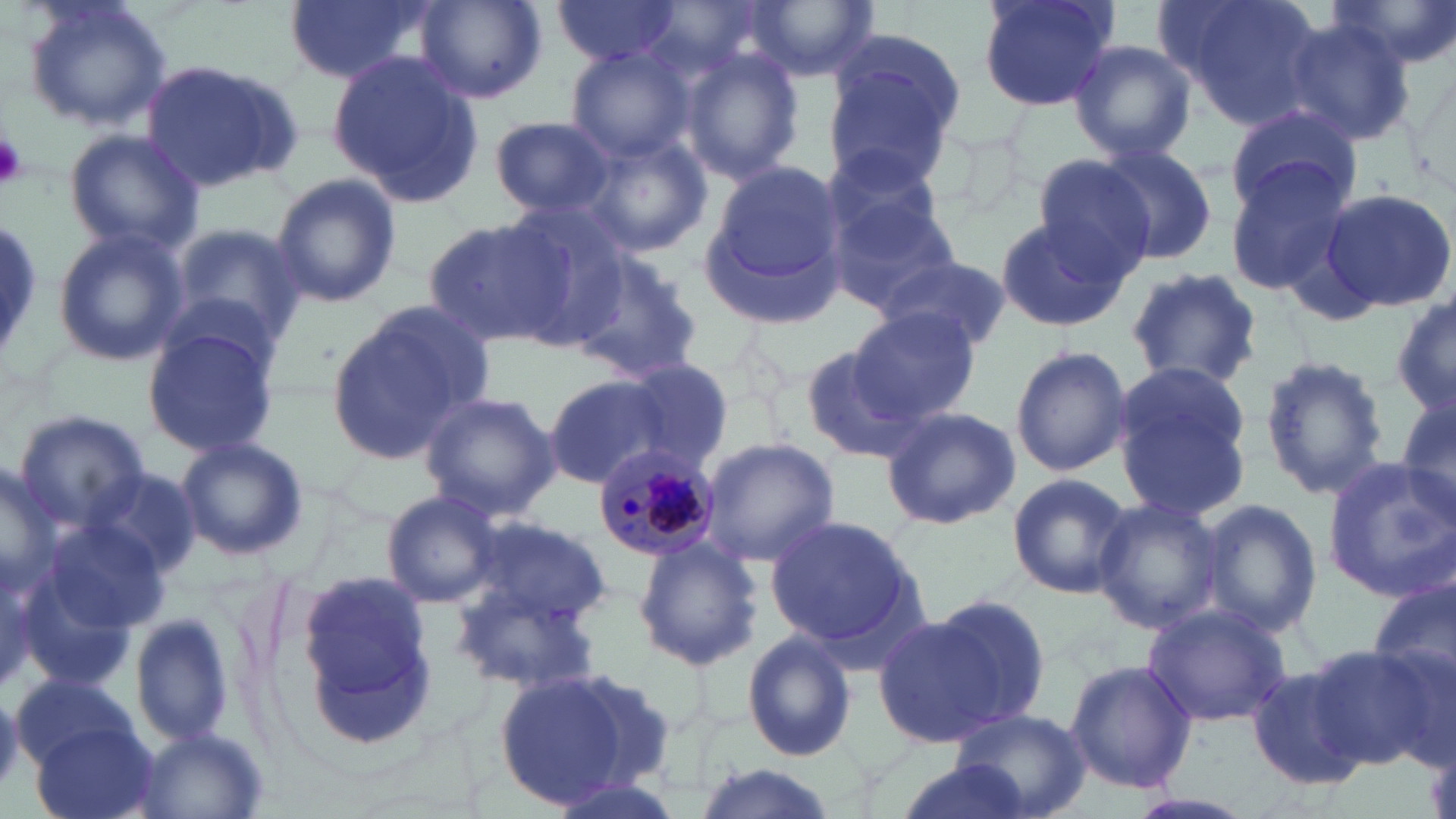
{
  "slide_level_diagnosis": "Plasmodium malariae",
  "uninfected_red_blood_cell_locations": "approximate bounding boxes as (x1, y1, x2, y2) in pixels: (23, 0, 170, 132), (282, 0, 432, 86), (415, 0, 549, 105), (551, 0, 685, 68), (975, 0, 1121, 112), (1159, 0, 1325, 127), (1334, 0, 1456, 70), (747, 1, 878, 82), (1277, 14, 1415, 150), (824, 33, 965, 176), (1067, 39, 1197, 163), (563, 45, 697, 164), (677, 46, 805, 184), (327, 51, 479, 205), (139, 58, 296, 196), (1223, 105, 1361, 213), (489, 116, 618, 218), (64, 131, 203, 254), (578, 132, 713, 257), (1088, 141, 1216, 267), (816, 143, 953, 263), (1032, 151, 1164, 279), (695, 158, 850, 328), (1224, 163, 1357, 295), (269, 172, 402, 308), (1317, 186, 1456, 316), (824, 189, 963, 313), (495, 205, 631, 348), (992, 214, 1131, 333), (422, 217, 574, 348), (0, 219, 42, 368), (170, 219, 309, 349), (51, 227, 189, 366), (571, 250, 706, 377), (879, 255, 1012, 352), (1124, 267, 1265, 391), (1390, 293, 1455, 419), (321, 303, 481, 465), (849, 307, 982, 424), (141, 321, 282, 458), (797, 341, 923, 466), (1010, 345, 1134, 476), (1259, 353, 1389, 502), (611, 360, 733, 472), (1112, 361, 1252, 515), (544, 374, 670, 488), (417, 391, 560, 520), (1393, 393, 1456, 522), (879, 405, 1021, 530), (15, 409, 151, 535), (175, 436, 310, 563), (698, 438, 840, 566), (1321, 458, 1456, 602), (0, 463, 63, 604), (84, 467, 204, 584), (1007, 472, 1133, 600), (381, 489, 508, 609), (1090, 496, 1225, 634), (1196, 497, 1322, 639), (464, 515, 613, 632), (763, 515, 923, 653), (41, 521, 170, 639), (632, 537, 763, 671), (295, 567, 437, 738), (1368, 575, 1456, 711), (449, 583, 602, 696), (930, 592, 1052, 727), (1141, 605, 1290, 725), (871, 610, 1015, 750), (130, 612, 238, 747), (741, 631, 858, 761), (1300, 641, 1445, 768), (1063, 658, 1198, 794), (1247, 664, 1370, 790), (489, 666, 654, 809), (12, 672, 139, 772), (951, 707, 1091, 819), (33, 722, 160, 819), (135, 728, 270, 819), (888, 759, 1036, 819), (690, 762, 842, 819), (1125, 791, 1260, 819)",
  "plasmodium_malariae_infected_red_blood_cell_locations": "approximate bounding boxes as (x1, y1, x2, y2) in pixels: (591, 443, 718, 564)",
  "field_of_view": "single",
  "preparation": "thin blood film",
  "stain": "May-Grünwald-Giemsa",
  "magnification": "1000x",
  "image_size": "1456×819 pixels",
  "modality": "optical microscopy",
  "platelet_locations": "approximate bounding boxes as (x1, y1, x2, y2) in pixels: (0, 131, 26, 189)"
}